Evaluate for Plasmodium parasites.
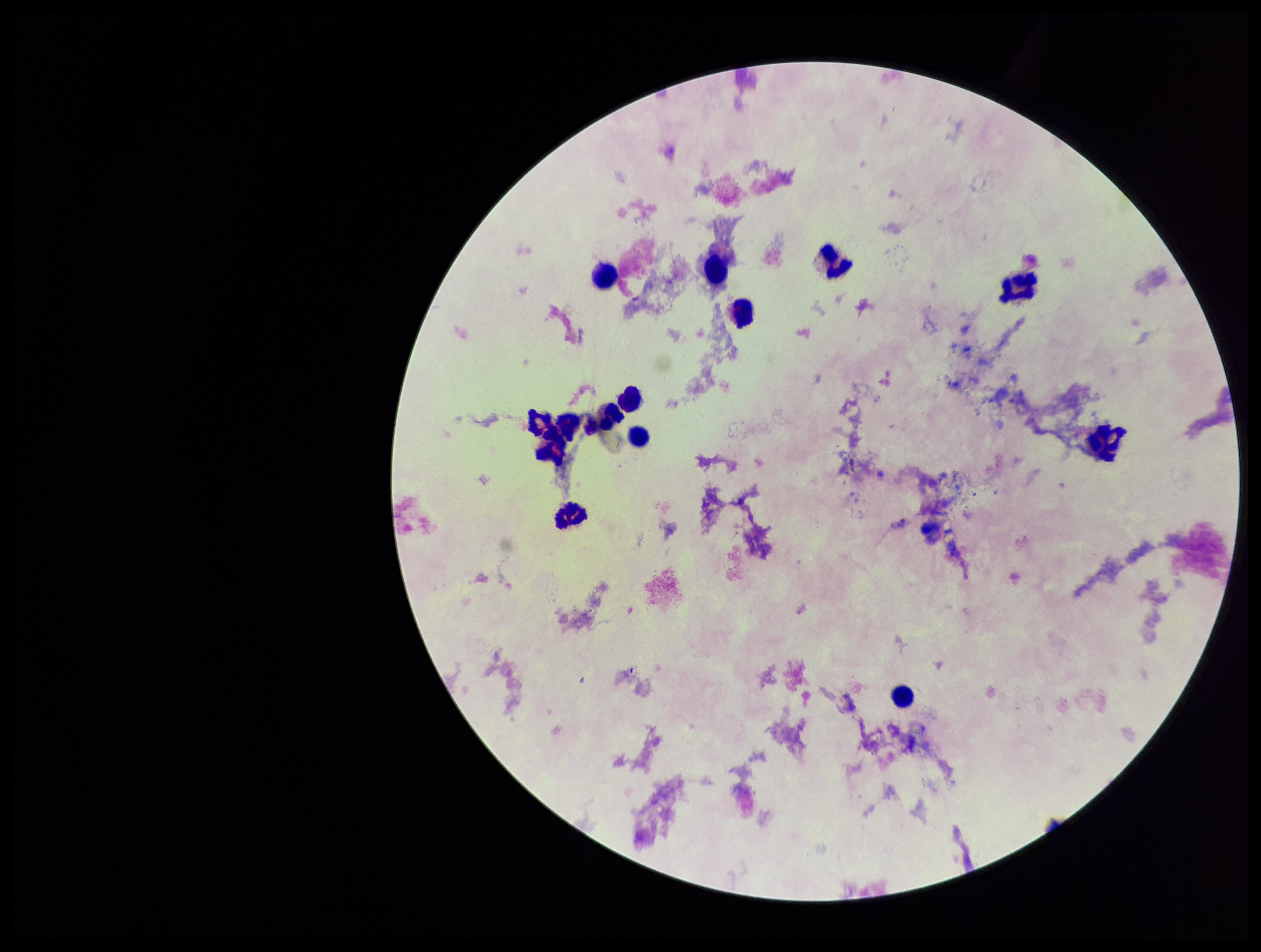

None seen.

Giemsa stain. Leukocyte count: 13. Photographed through the microscope eyepiece with a smartphone camera. Image is 1261×952 pixels. Patient malaria status: negative. Parasite count: 0. One field from this slide. Preparation: thick blood smear.